Locate and identify every blood parasite.
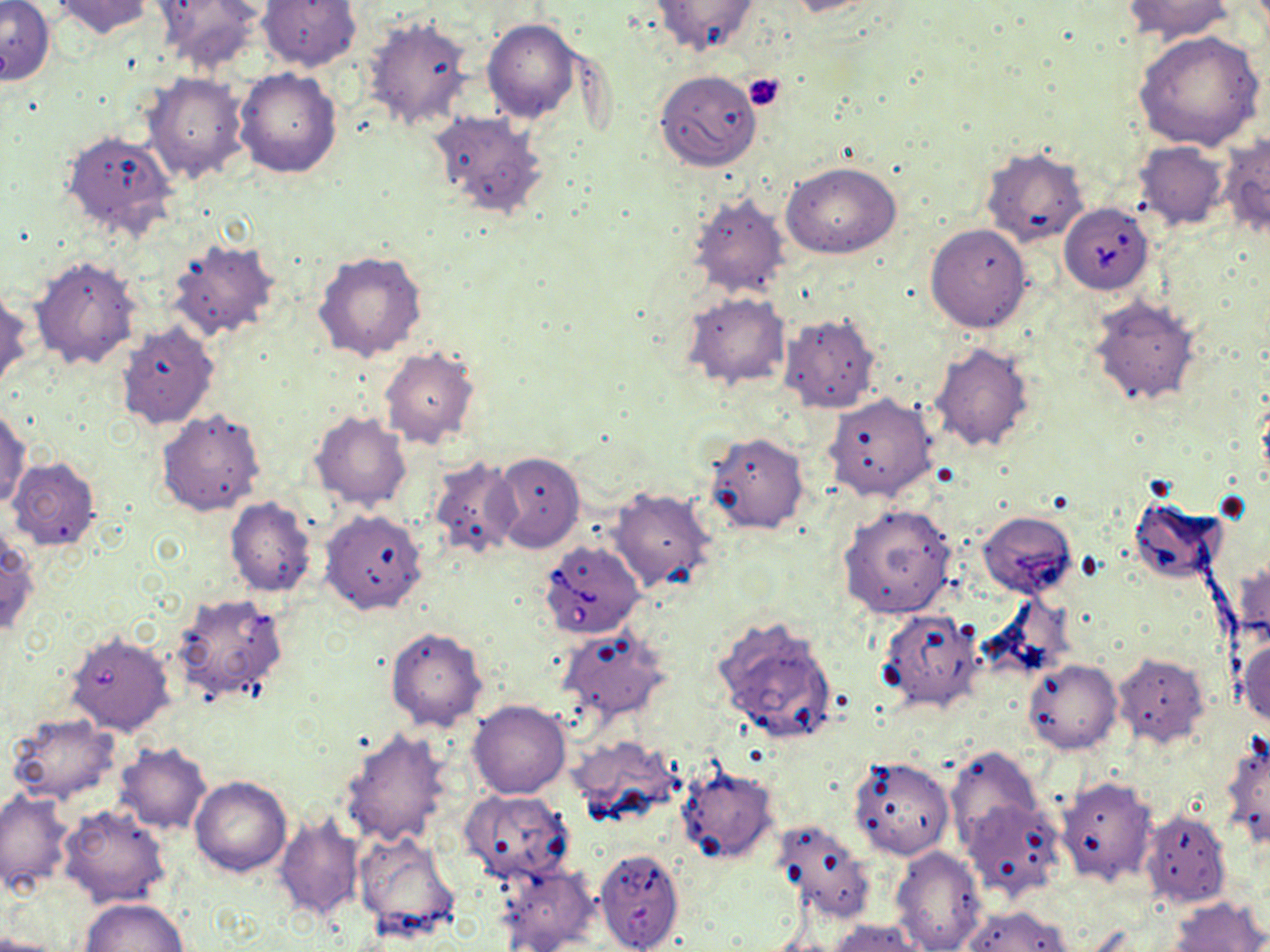
Approximate bounding boxes as [x1, y1, x2, y2] in pixels.
Babesia divergens-infected red blood cells: [1059, 204, 1152, 294], [539, 540, 645, 638].
No Plasmodium falciparum, Plasmodium ovale, Plasmodium malariae, Plasmodium vivax, or Trypanosoma brucei observed.

slide-level diagnosis = Babesia divergens
preparation = thin blood smear
field of view = one of a larger specimen
modality = optical microscopy
image size = 1270×952 pixels
uninfected red blood cell locations = approximate bounding boxes as [x1, y1, x2, y2] in pixels: [49, 0, 155, 39], [149, 0, 266, 75], [256, 0, 360, 72], [647, 0, 761, 58], [781, 0, 891, 17], [1123, 0, 1235, 44], [1, 1, 53, 86], [363, 15, 476, 132], [482, 18, 581, 123], [1133, 31, 1265, 151], [234, 67, 343, 178], [654, 70, 762, 171], [142, 72, 250, 184], [429, 110, 548, 219], [60, 129, 179, 242], [1218, 132, 1270, 238], [1134, 141, 1229, 231], [980, 146, 1090, 249], [782, 162, 901, 258], [686, 188, 793, 300], [925, 223, 1032, 333], [166, 238, 281, 342], [313, 251, 428, 362], [28, 254, 143, 370], [0, 285, 32, 393], [680, 292, 792, 392], [1087, 295, 1201, 406], [777, 312, 880, 414], [117, 323, 219, 430], [928, 341, 1035, 454], [378, 346, 481, 450], [824, 393, 938, 502], [0, 404, 31, 509], [156, 408, 266, 518], [309, 410, 413, 511], [702, 431, 810, 535], [491, 451, 584, 554], [424, 456, 524, 561], [7, 457, 102, 552], [606, 485, 718, 595], [1130, 495, 1227, 587], [224, 498, 317, 597], [838, 503, 958, 619], [320, 509, 428, 615], [977, 511, 1076, 599], [0, 531, 38, 639], [1233, 559, 1270, 651], [170, 590, 289, 705], [876, 607, 984, 712], [712, 614, 838, 746], [385, 626, 487, 730], [554, 626, 670, 725], [64, 630, 174, 736], [1235, 635, 1270, 729], [1112, 652, 1210, 747], [1024, 658, 1122, 753], [467, 700, 571, 799], [5, 712, 121, 804], [338, 727, 453, 848], [571, 733, 682, 825], [1221, 737, 1270, 851], [114, 743, 212, 835], [945, 747, 1044, 851], [849, 756, 955, 860], [674, 764, 779, 866], [1054, 775, 1157, 887], [190, 776, 291, 879], [0, 788, 74, 894], [460, 789, 574, 883], [960, 798, 1065, 903], [58, 804, 172, 909], [274, 808, 366, 923], [1141, 809, 1231, 907], [769, 816, 878, 925], [354, 830, 460, 941], [890, 845, 987, 952], [594, 847, 685, 952], [495, 858, 601, 952], [1168, 897, 1268, 952], [80, 898, 188, 951], [961, 905, 1074, 952], [827, 918, 923, 952], [0, 936, 64, 952]
platelet locations = approximate bounding boxes as [x1, y1, x2, y2] in pixels: [742, 73, 786, 111]
magnification = 1000x
stain = May-Grünwald-Giemsa